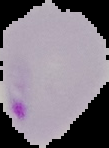
preparation = thin blood film
result = Plasmodium parasites identified
image type = cell region segmented out of the field of view; surrounding area masked to black
image size = 109×148 pixels